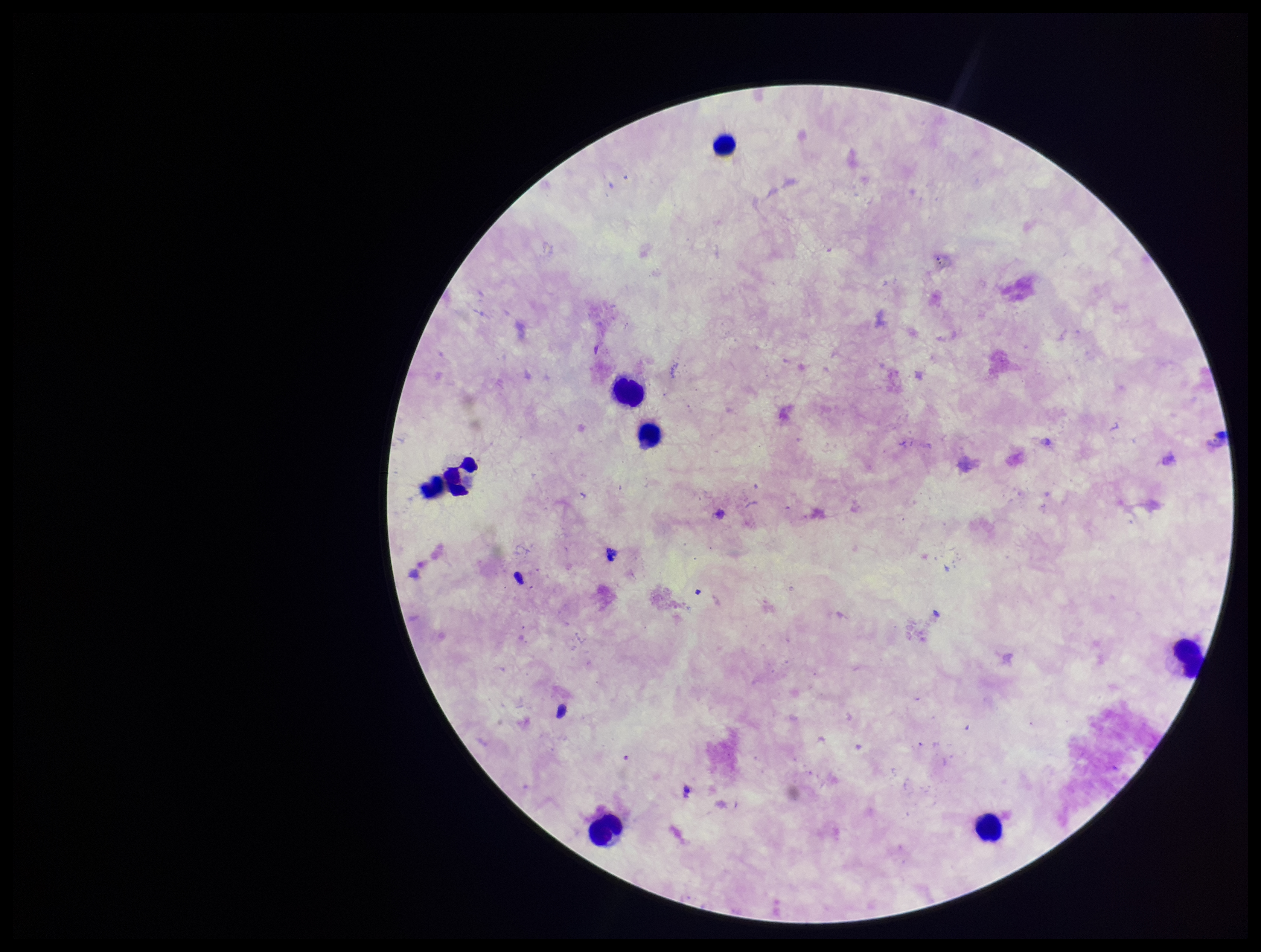
Summary:
  - Stain: Giemsa
  - Image size: 1261×952 pixels
  - Capture: smartphone photograph through the microscope eyepiece
  - Field of view: one from this slide
  - Plasmodium parasites: none identified
  - Patient malaria status: negative
  - Parasite count: 0
  - Leukocyte count: 7
  - Preparation: thick smear